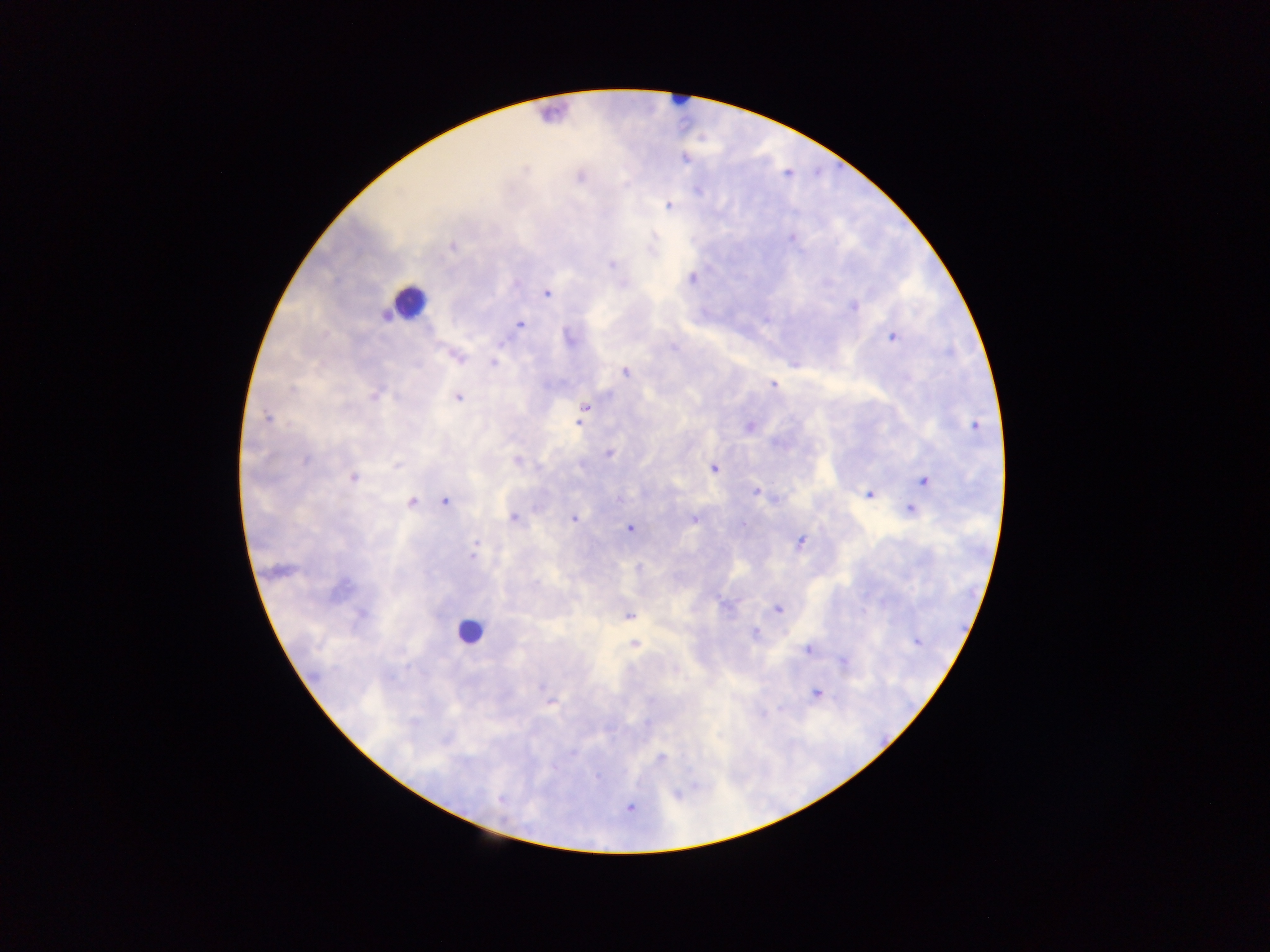 Approximate centers as (x, y) in pixels. Leukocyte locations: (409, 301), (468, 632). Plasmodium parasite locations: (684, 159), (580, 176), (698, 190), (668, 206), (792, 238), (453, 246), (611, 264), (692, 278), (546, 294), (853, 306), (521, 324), (893, 337), (570, 340), (502, 343), (457, 357), (494, 363), (625, 372), (773, 383), (292, 388), (374, 397), (458, 397), (585, 407), (267, 417), (579, 423), (749, 427), (975, 427), (609, 454), (306, 460), (517, 460), (397, 465), (714, 468), (353, 478), (924, 481), (755, 492), (869, 495), (619, 498), (445, 501), (412, 502), (910, 509), (513, 517), (574, 519), (693, 519), (744, 524), (629, 528), (799, 543), (473, 554), (724, 605), (777, 609), (362, 614), (629, 616), (755, 633), (917, 642), (634, 644), (807, 650), (843, 661), (542, 687), (816, 693), (550, 703), (572, 753), (661, 758), (598, 777), (694, 787), (676, 794), (500, 800), (629, 808). Photographed through a microscope with a mobile-phone camera. One field of view. Collected in Ghana. Image is 1270×952 pixels. Thick blood smear.